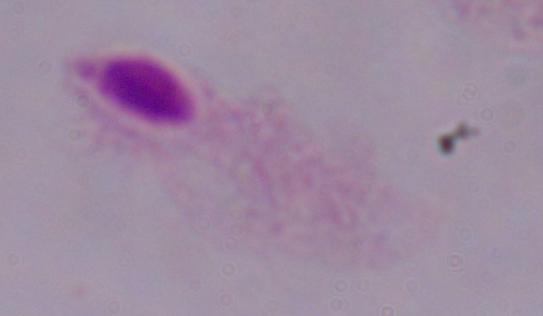
Micrograph. Captured at 1000x magnification. A trichomonad is shown.